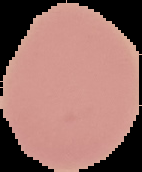

Image is 142×172 pixels. Result: negative for Plasmodium parasites. Cell region segmented out of the field of view; the surrounding area is masked to black. From a thin blood smear.